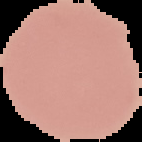

image size = 142×142 pixels
preparation = thin blood film
malaria status = uninfected
image type = segmented cell region with the area outside set to black